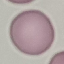

Malaria status: uninfected. Thin smear of blood. Giemsa-stained preparation. Automatically extracted cell patch, resized to 64 × 64 pixels. Photographed with a smartphone camera at the microscope eyepiece.